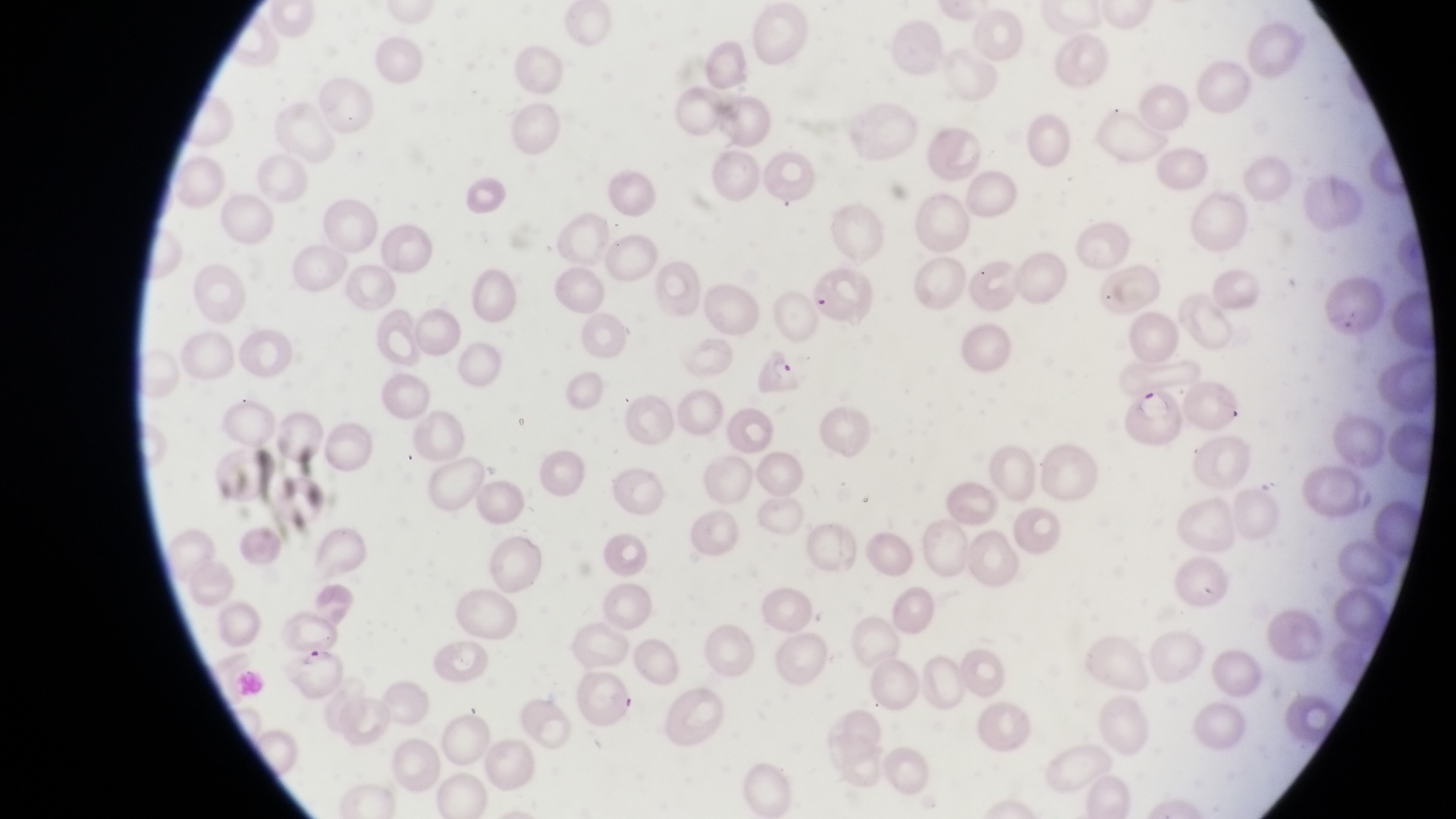

Approximate bounding boxes as left top right bottom in pixels. Parasitised red blood cell locations: 809 265 878 328; 753 338 805 398; 1123 377 1183 444; 285 647 352 710. Captured by a smartphone held over the eyepiece of an Olympus CX-23 microscope. Sample from Uganda. Thin blood smear. Image is 1456×819 pixels. At a magnification of 1000x. One field of view.